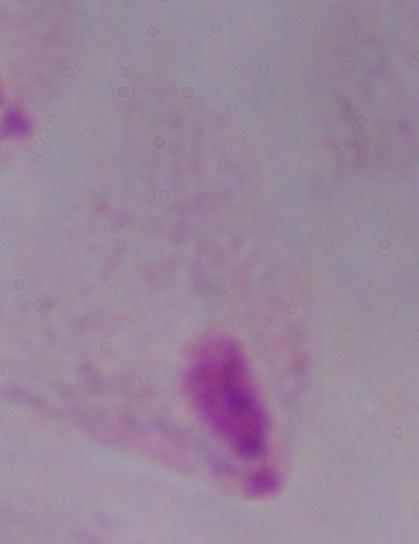

A trichomonad is seen. 1000x magnification. Micrograph.